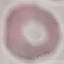 Malaria status: uninfected. Giemsa-stained preparation. Acquired by smartphone through the microscope eyepiece. Thin blood film. Cell patch, automatically extracted from a larger field of view and resized to 64 × 64 pixels.